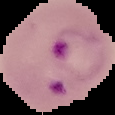

Summary:
  - Image type: cell region segmented out of the field of view; surrounding area masked to black
  - Preparation: thin blood film
  - Malaria status: parasitized
  - Image size: 115×115 pixels